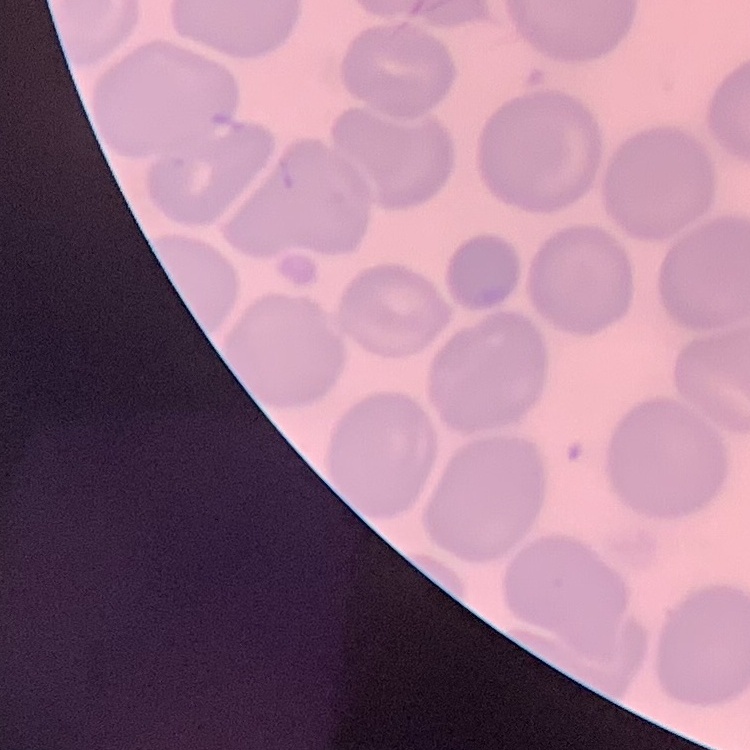
erythrocyte morphology = no rouleaux formation
preparation = thin blood film
stain = Field's or Giemsa
image type = square crop of a larger photomicrograph